Name the parasite shown.
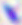
Toxoplasma gondii.

magnification = 400x
modality = photomicrograph